Evaluate for malaria.
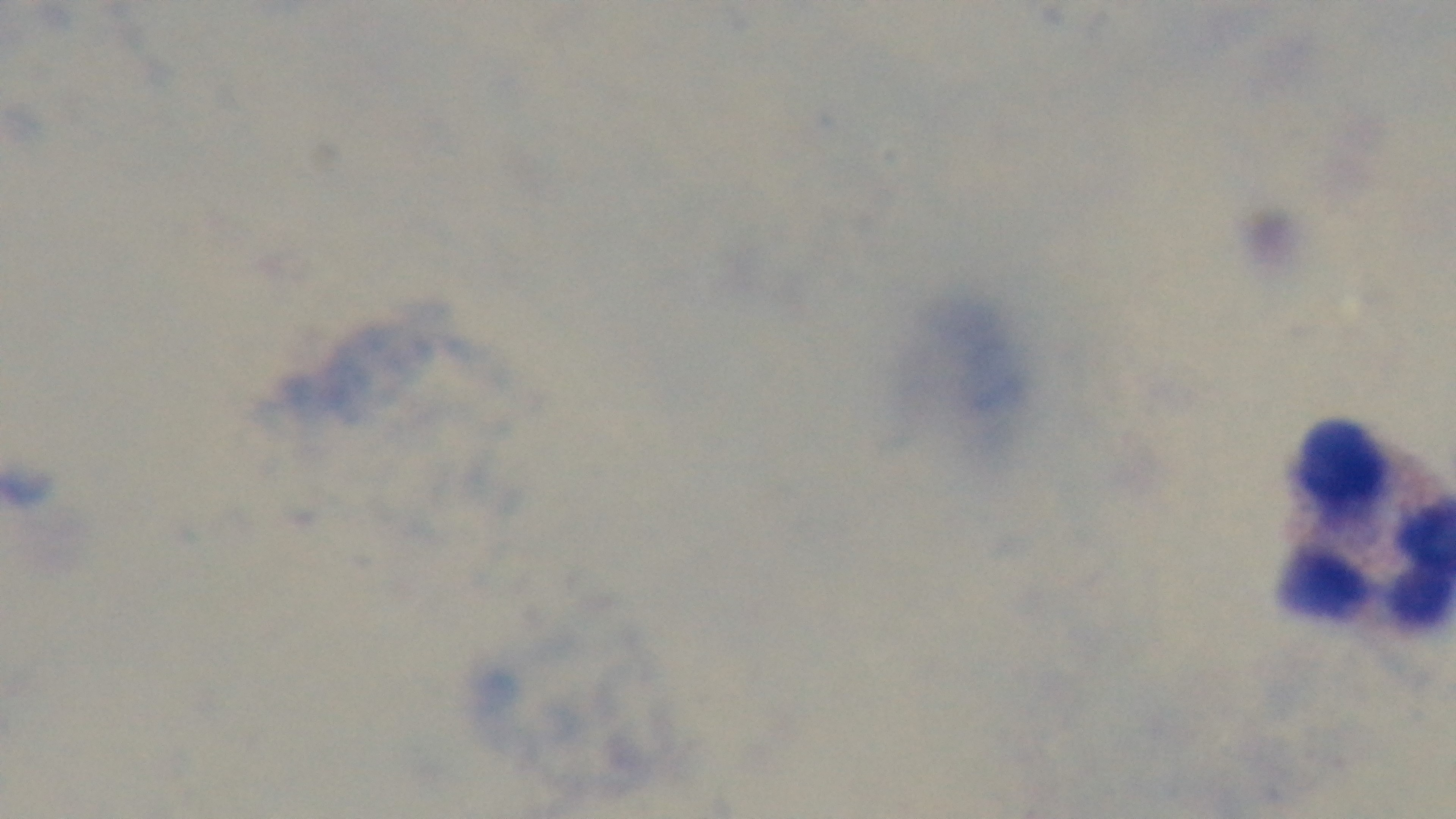

It is uninfected.

Captured with a mounted 4K digital camera. Giemsa stain. Preparation: thick. Oil-immersion objective, 100x. Light microscopy. Single field of view.